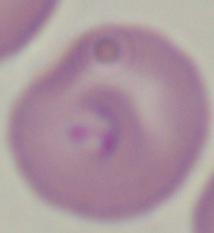
Summary:
  - Magnification: 1000x
  - Identification: Babesia
  - Modality: photomicrograph